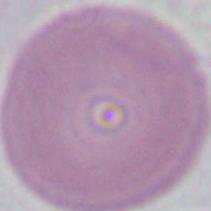

{
  "modality": "micrograph",
  "magnification": "1000x",
  "identification": "erythrocyte"
}